Assess this cell for malaria.
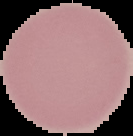

It is uninfected.

preparation: thin blood smear
image_type: segmented cell region with the area outside set to black
image_size: 133×136 pixels